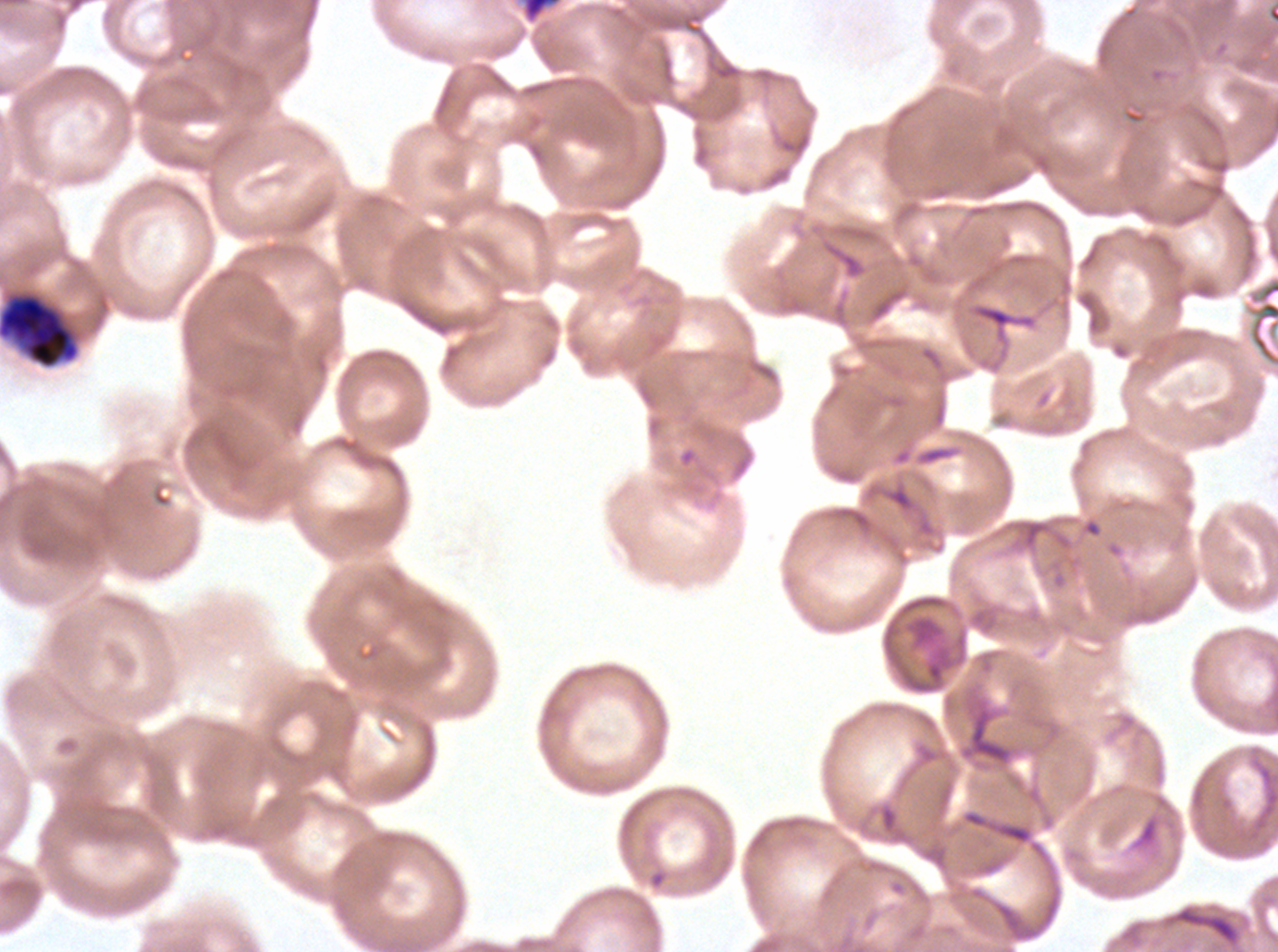

notation = approximate bounding boxes as (x1, y1, x2, y2) in pixels
late schizont locations = (520, 0, 563, 25)
early schizont locations = (0, 293, 79, 369)
life-cycle stages observed = early schizont, late schizont
preparation = thin blood film
stain = Giemsa
specimen = ex-vivo Plasmodium falciparum culture from a patient in The Gambia, grown for 24 to 48 hours
image size = 1278×952 pixels
field of view = sub-image separated from a larger composite